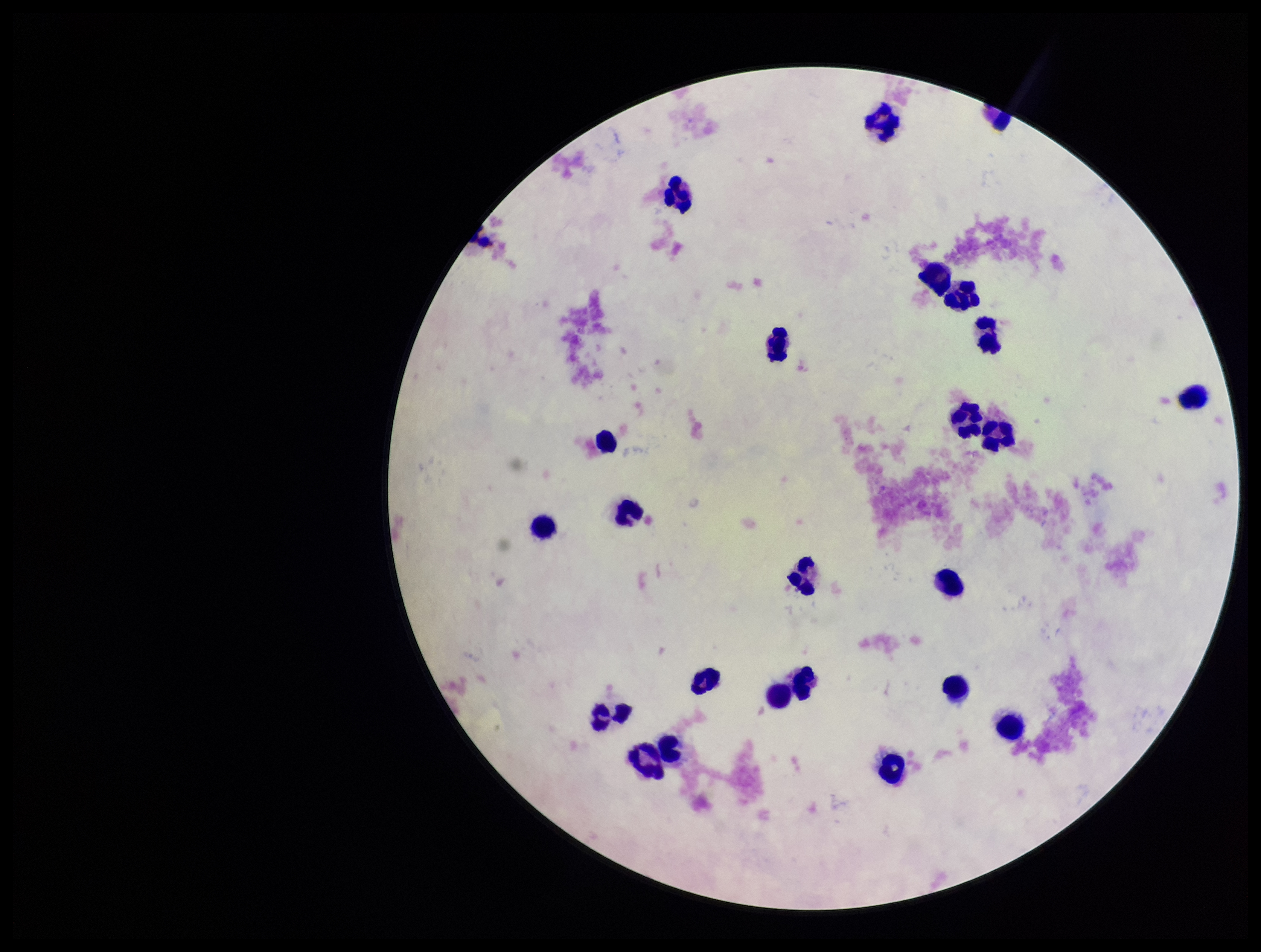
Summary:
  - Leukocyte count: 24
  - Capture: smartphone photograph through the microscope eyepiece
  - Plasmodium parasites: none seen
  - Parasite count: 0
  - Stain: Giemsa
  - Preparation: thick smear
  - Field of view: one from this slide
  - Image size: 1261×952 pixels
  - Patient malaria status: negative